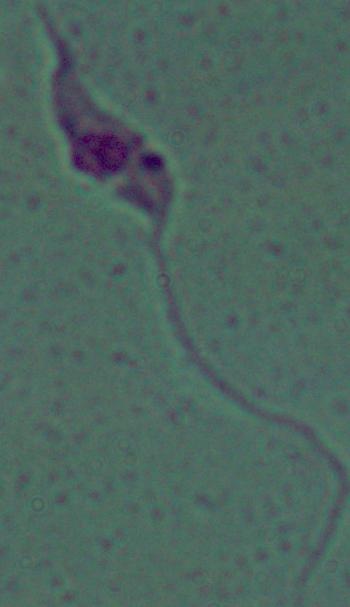
identification = Leishmania
modality = micrograph
magnification = 1000x